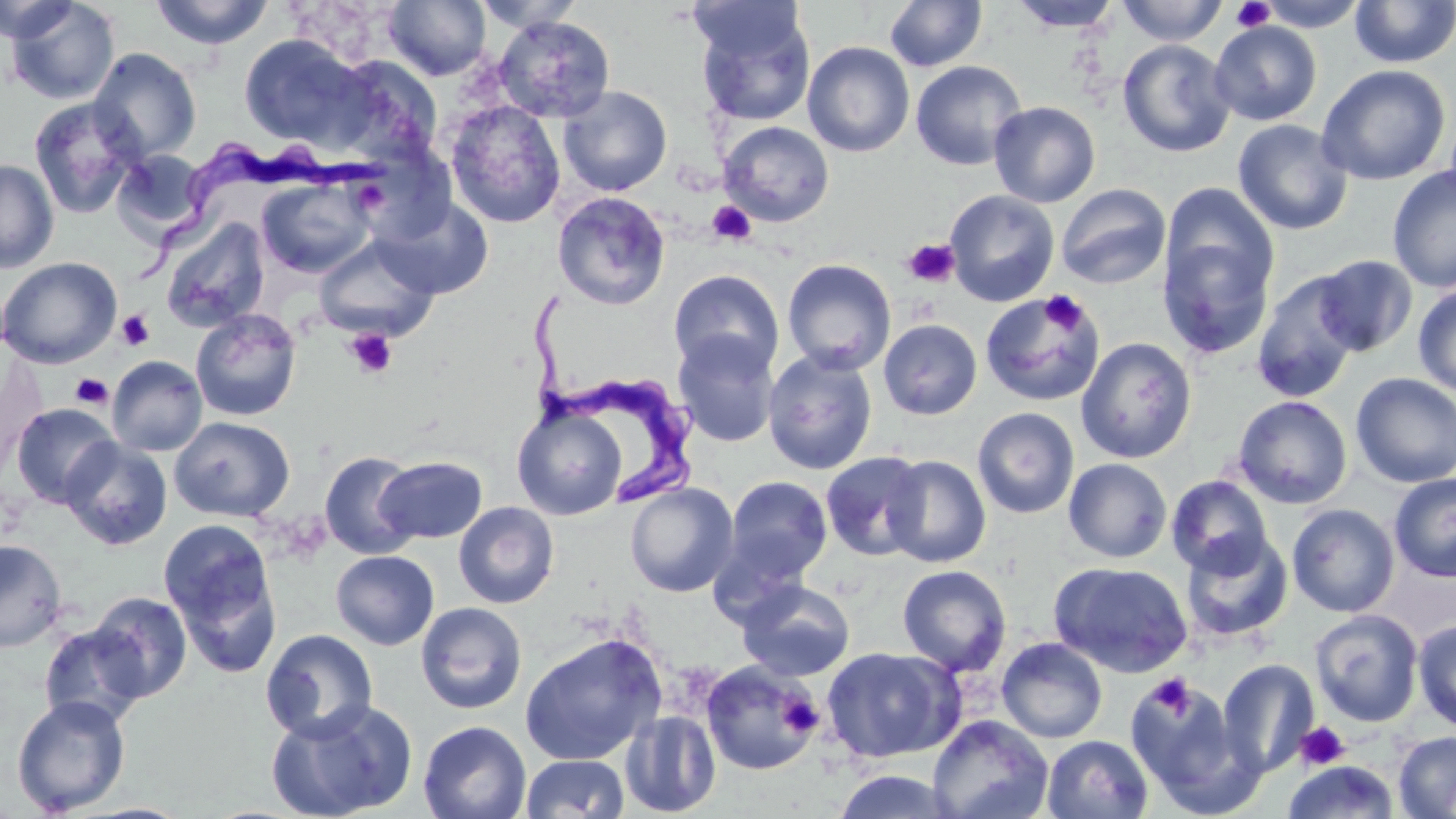

Summary:
  - Coordinate format: approximate bounding boxes as named x1/y1/x2/y2 corners in pixels
  - Platelet locations: (x1=1230, y1=0, x2=1276, y2=32), (x1=707, y1=201, x2=756, y2=246), (x1=901, y1=238, x2=961, y2=289), (x1=1040, y1=290, x2=1088, y2=334), (x1=116, y1=310, x2=155, y2=351), (x1=345, y1=329, x2=399, y2=379), (x1=71, y1=373, x2=114, y2=408), (x1=1146, y1=674, x2=1194, y2=718), (x1=777, y1=693, x2=824, y2=737), (x1=1294, y1=721, x2=1350, y2=770)
  - Trypanosoma brucei locations: (x1=141, y1=139, x2=391, y2=290), (x1=527, y1=287, x2=709, y2=510)
  - Uninfected red blood cell locations: (x1=0, y1=0, x2=80, y2=44), (x1=4, y1=0, x2=120, y2=105), (x1=1009, y1=0, x2=1123, y2=32), (x1=1116, y1=0, x2=1228, y2=46), (x1=1254, y1=0, x2=1370, y2=31), (x1=147, y1=1, x2=277, y2=50), (x1=383, y1=1, x2=492, y2=81), (x1=472, y1=1, x2=586, y2=34), (x1=884, y1=1, x2=987, y2=72), (x1=1349, y1=1, x2=1456, y2=68), (x1=692, y1=3, x2=815, y2=127), (x1=1336, y1=4, x2=1456, y2=148), (x1=493, y1=15, x2=616, y2=124), (x1=1209, y1=20, x2=1322, y2=126), (x1=238, y1=34, x2=372, y2=150), (x1=1117, y1=39, x2=1236, y2=157), (x1=802, y1=41, x2=915, y2=157), (x1=88, y1=48, x2=202, y2=163), (x1=329, y1=54, x2=443, y2=165), (x1=910, y1=60, x2=1027, y2=170), (x1=1316, y1=64, x2=1451, y2=186), (x1=558, y1=86, x2=673, y2=196), (x1=28, y1=97, x2=143, y2=218), (x1=445, y1=100, x2=566, y2=229), (x1=988, y1=101, x2=1101, y2=207), (x1=1232, y1=119, x2=1353, y2=235), (x1=718, y1=121, x2=834, y2=227), (x1=113, y1=150, x2=210, y2=240), (x1=0, y1=159, x2=59, y2=274), (x1=1387, y1=165, x2=1456, y2=292), (x1=256, y1=177, x2=376, y2=278), (x1=1159, y1=181, x2=1279, y2=301), (x1=1055, y1=183, x2=1172, y2=289), (x1=945, y1=189, x2=1060, y2=307), (x1=552, y1=191, x2=671, y2=311), (x1=374, y1=195, x2=494, y2=299), (x1=160, y1=217, x2=270, y2=332), (x1=1157, y1=234, x2=1275, y2=359), (x1=313, y1=236, x2=439, y2=341), (x1=1311, y1=254, x2=1418, y2=357), (x1=0, y1=256, x2=122, y2=369), (x1=782, y1=258, x2=897, y2=374), (x1=668, y1=269, x2=784, y2=378), (x1=1251, y1=272, x2=1362, y2=402), (x1=1413, y1=283, x2=1456, y2=397), (x1=978, y1=290, x2=1103, y2=408), (x1=190, y1=308, x2=302, y2=422), (x1=878, y1=318, x2=982, y2=420), (x1=672, y1=330, x2=780, y2=448), (x1=1076, y1=337, x2=1197, y2=463), (x1=762, y1=349, x2=878, y2=476), (x1=107, y1=355, x2=208, y2=456), (x1=1350, y1=373, x2=1456, y2=487), (x1=1232, y1=395, x2=1352, y2=509), (x1=10, y1=403, x2=121, y2=508), (x1=512, y1=403, x2=627, y2=520), (x1=972, y1=407, x2=1080, y2=519), (x1=170, y1=415, x2=295, y2=522), (x1=59, y1=438, x2=173, y2=550), (x1=320, y1=451, x2=421, y2=559), (x1=820, y1=451, x2=929, y2=561), (x1=882, y1=454, x2=991, y2=567), (x1=375, y1=455, x2=488, y2=544), (x1=1063, y1=458, x2=1173, y2=563), (x1=1389, y1=473, x2=1456, y2=582), (x1=724, y1=475, x2=833, y2=584), (x1=1166, y1=475, x2=1273, y2=577), (x1=625, y1=482, x2=739, y2=597), (x1=454, y1=501, x2=559, y2=608), (x1=1287, y1=504, x2=1400, y2=618), (x1=159, y1=518, x2=276, y2=638), (x1=1180, y1=531, x2=1293, y2=643), (x1=0, y1=539, x2=67, y2=652), (x1=331, y1=550, x2=439, y2=650), (x1=171, y1=556, x2=284, y2=680), (x1=1049, y1=560, x2=1193, y2=677), (x1=897, y1=564, x2=1012, y2=676), (x1=737, y1=579, x2=855, y2=682), (x1=87, y1=591, x2=193, y2=702), (x1=416, y1=602, x2=527, y2=714), (x1=1310, y1=608, x2=1424, y2=727), (x1=1413, y1=619, x2=1456, y2=732), (x1=38, y1=622, x2=150, y2=729), (x1=260, y1=628, x2=378, y2=742), (x1=519, y1=632, x2=668, y2=765), (x1=997, y1=637, x2=1108, y2=743), (x1=821, y1=647, x2=962, y2=763), (x1=1217, y1=659, x2=1319, y2=778), (x1=701, y1=660, x2=822, y2=776), (x1=1124, y1=675, x2=1244, y2=804), (x1=11, y1=695, x2=131, y2=815), (x1=265, y1=698, x2=418, y2=819), (x1=620, y1=709, x2=721, y2=817), (x1=927, y1=715, x2=1053, y2=819), (x1=417, y1=720, x2=532, y2=819), (x1=1393, y1=731, x2=1456, y2=819), (x1=1041, y1=734, x2=1153, y2=819), (x1=520, y1=753, x2=630, y2=818), (x1=1283, y1=760, x2=1399, y2=818), (x1=831, y1=769, x2=962, y2=818)
  - Slide-level diagnosis: Trypanosoma brucei
  - Image size: 1456×819 pixels
  - Stain: May-Grünwald-Giemsa
  - Modality: light microscopy
  - Magnification: 1000x
  - Field of view: one of a larger specimen
  - Preparation: thin blood film